Locate Plasmodium parasites and leukocytes.
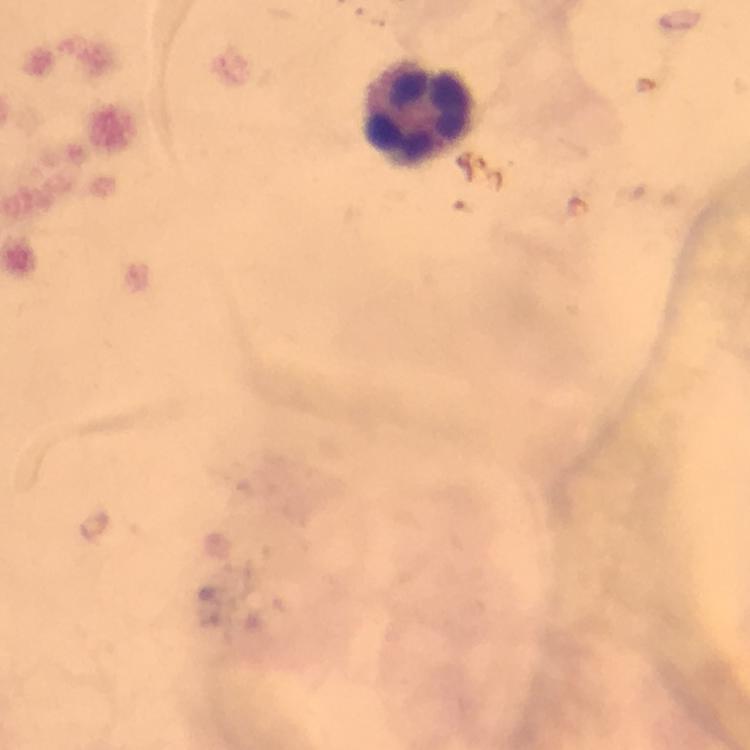

No Plasmodium parasites seen.
Approximate centers as [x, y] in pixels.
Leukocytes: [420, 115].

cropped from = one field of view
context = from a malaria diagnostic workup
immersion oil = applied
image size = 750×750 pixels
preparation = thick blood smear
magnification = 100x
capture = smartphone camera through the microscope
stain = Giemsa